Report the malaria status of this cell.
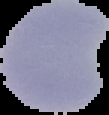

It is parasitized.

image_size: 109×115 pixels
image_type: segmented cell region with the area outside set to black
preparation: thin blood smear